Comment on the morphology of the red blood cells.
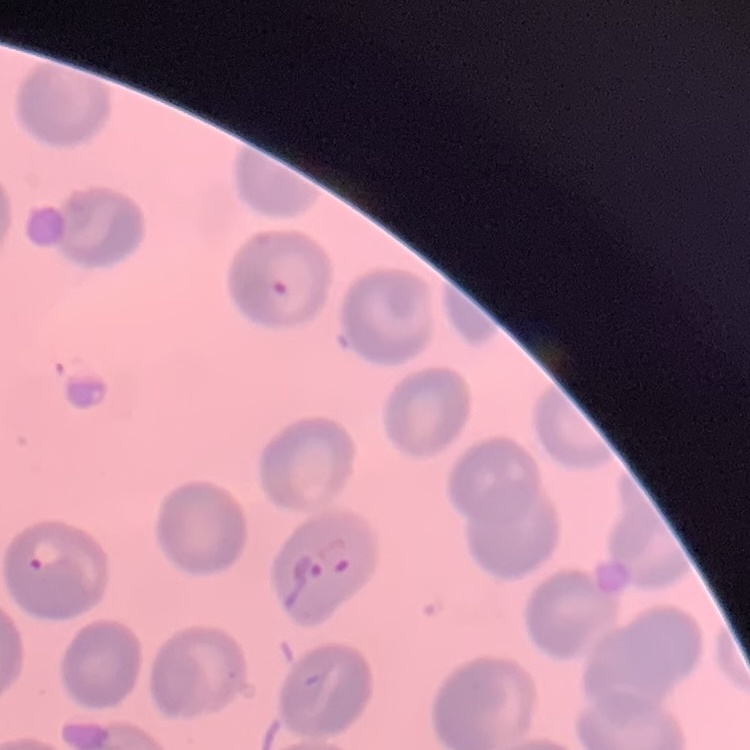

No rouleaux formation.

Summary:
  - Image type: one tile cut from a larger photomicrograph
  - Preparation: thin blood smear
  - Stain: Field's or Giemsa